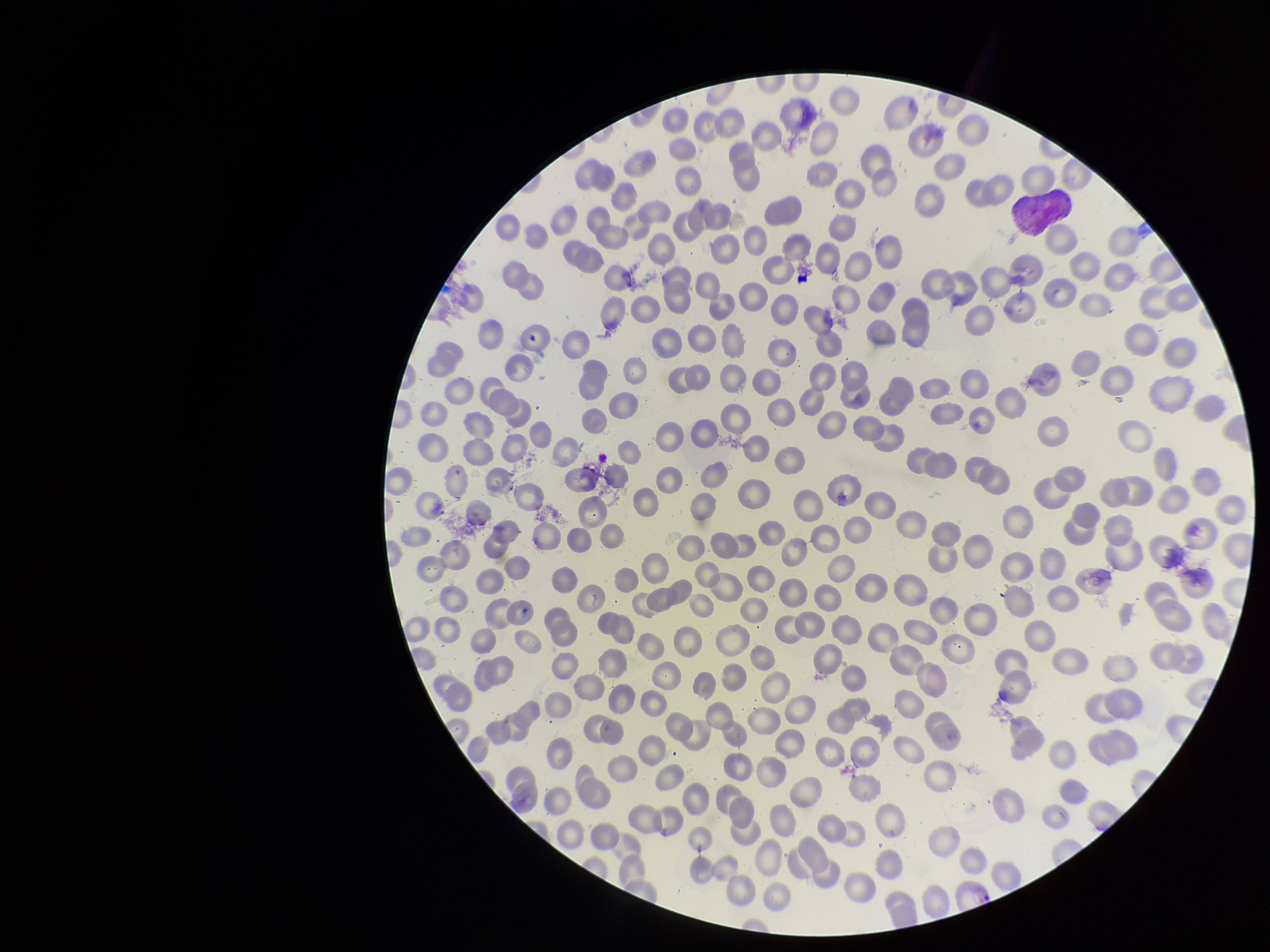
{
  "field_of_view": "single",
  "parasitized_red_blood_cells": "identified",
  "preparation": "thin blood smear",
  "species_reported_for_this_patient": "Plasmodium vivax",
  "patient_malaria_status": "infected",
  "capture": "smartphone photograph through the microscope eyepiece",
  "stain": "Giemsa",
  "red_blood_cell_count": 288,
  "image_size": "1270×952 pixels",
  "parasitized_red_blood_cell_count": 1
}